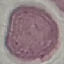
Malaria status: uninfected. Photographed with a smartphone camera at the microscope eyepiece. Thin smear of blood. Giemsa stain. Automatically extracted cell patch, resized to 64 × 64 pixels.